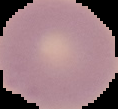
Summary:
  - Preparation: thin blood smear
  - Malaria status: uninfected
  - Image size: 118×109 pixels
  - Image type: cell region segmented out of the field of view; surrounding area masked to black